Assess this cell for malaria.
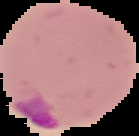

Parasitized.

Summary:
  - Image type: segmented cell region on a black background
  - Preparation: thin blood smear
  - Image size: 139×136 pixels